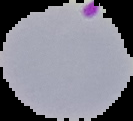
image type = segmented cell region on a black background
preparation = thin blood smear
malaria status = parasitized
image size = 133×121 pixels